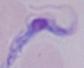
Summary:
  - Modality: photomicrograph
  - Identification: trypanosome
  - Magnification: 1000x